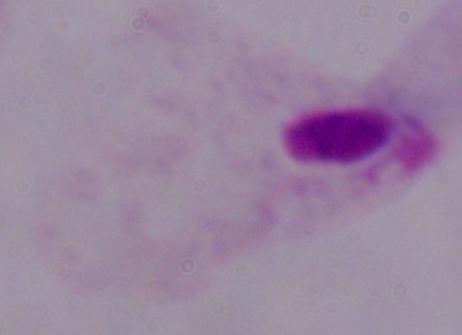
Summary:
  - Magnification: 1000x
  - Modality: photomicrograph
  - Identification: trichomonad